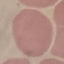

Summary:
  - Result: no malaria parasites detected
  - Image type: cell patch, automatically extracted from a larger field of view and resized to 64 × 64 pixels
  - Stain: Giemsa
  - Capture: smartphone camera at the microscope eyepiece
  - Preparation: thin blood smear